Comment on the morphology of the red blood cells.
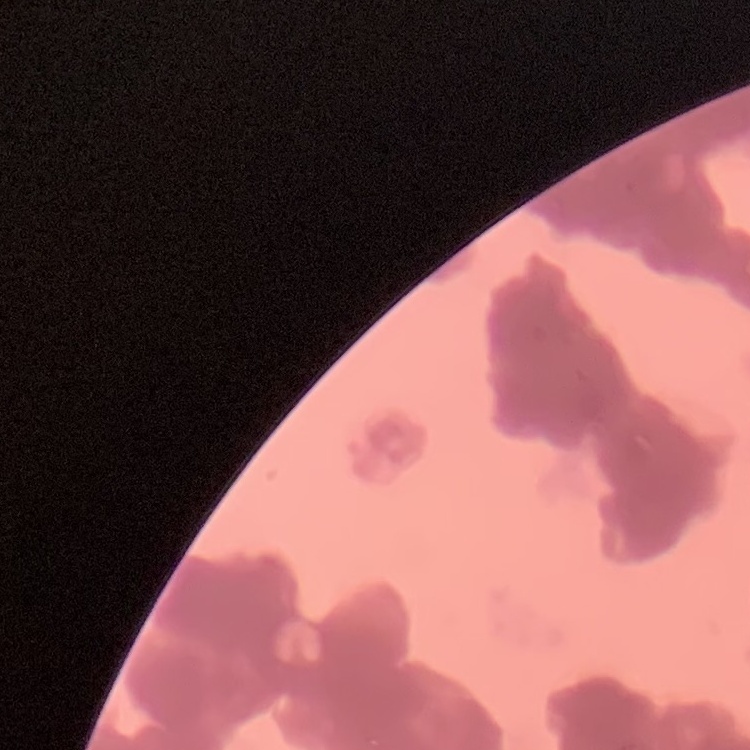

They show rouleaux formation.

One tile cut from a larger photomicrograph. Thin blood smear. Stained with either Field's or Giemsa.